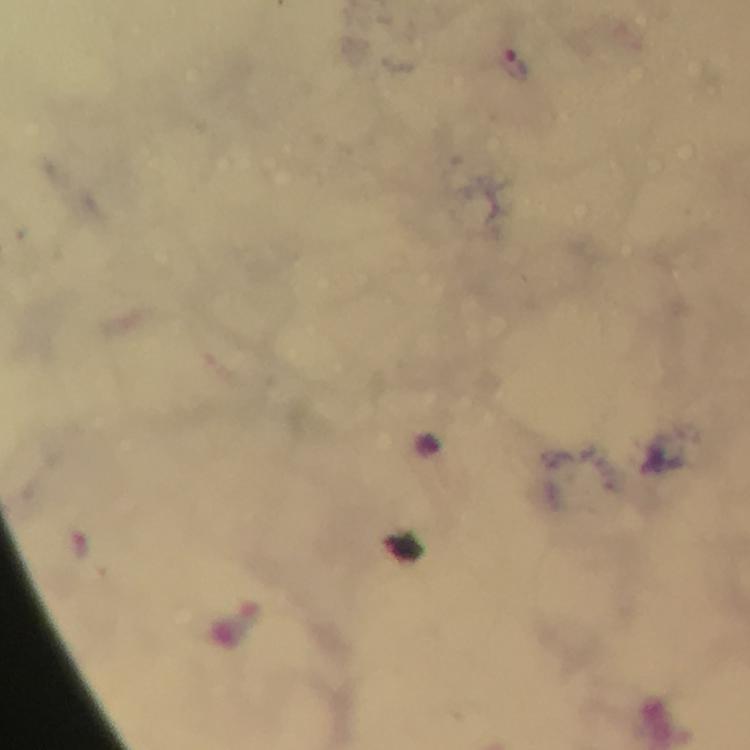
{
  "magnification": "100x",
  "immersion_oil": "used",
  "preparation": "thick blood smear",
  "context": "from a diagnostic examination for malaria",
  "capture": "smartphone mounted on the microscope",
  "stain": "Giemsa",
  "image_size": "750×750 pixels",
  "malaria_parasite_locations": "approximate centers as [x, y] in pixels: [515, 62]",
  "cropped_from": "one field of view"
}